Locate every Plasmodium falciparum-infected red blood cell.
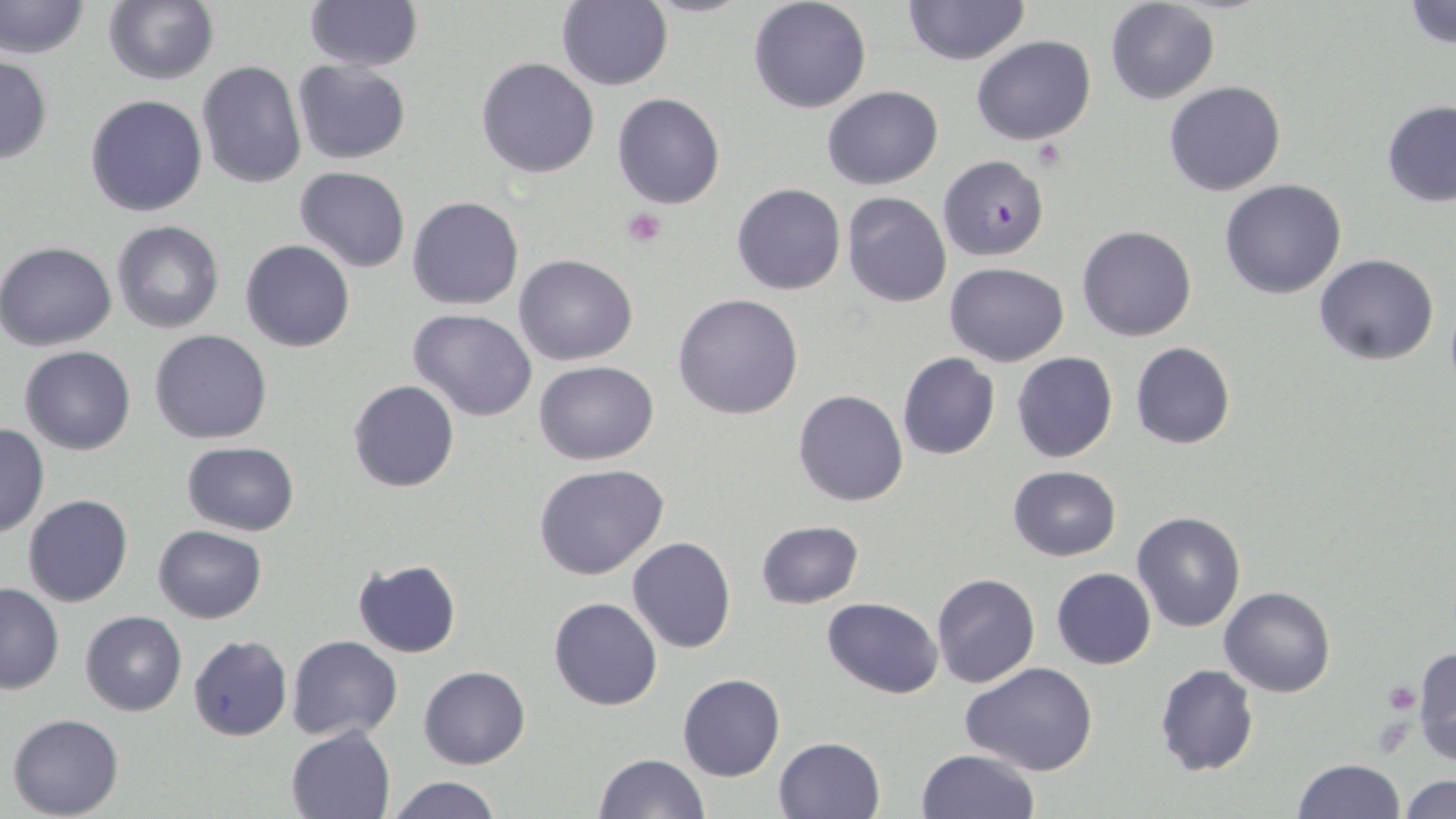

Approximate bounding boxes as (x1, y1, x2, y2) in pixels.
Plasmodium falciparum-infected red blood cells: (937, 155, 1049, 261).

slide-level diagnosis = Plasmodium falciparum
preparation = thin blood film
stain = May-Grünwald-Giemsa
image size = 1456×819 pixels
modality = optical microscopy
platelet locations = approximate bounding boxes as (x1, y1, x2, y2) in pixels: (622, 206, 666, 248), (1382, 680, 1421, 712)
uninfected red blood cell locations = approximate bounding boxes as (x1, y1, x2, y2) in pixels: (0, 0, 89, 60), (748, 0, 872, 113), (904, 0, 1029, 66), (303, 1, 422, 72), (556, 1, 672, 91), (1105, 1, 1219, 104), (1403, 1, 1456, 51), (102, 2, 218, 85), (971, 34, 1096, 144), (0, 53, 52, 163), (476, 57, 600, 178), (196, 59, 305, 188), (292, 61, 411, 164), (1164, 80, 1286, 196), (823, 86, 943, 189), (612, 93, 724, 208), (84, 94, 207, 216), (1381, 102, 1456, 206), (295, 165, 410, 273), (1218, 178, 1347, 299), (730, 182, 846, 295), (841, 192, 952, 308), (407, 195, 524, 310), (112, 221, 224, 334), (1077, 225, 1197, 342), (241, 240, 355, 352), (0, 241, 119, 351), (1314, 253, 1440, 366), (514, 254, 638, 366), (945, 262, 1069, 365), (673, 294, 804, 420), (408, 310, 538, 422), (150, 329, 274, 444), (1130, 342, 1236, 449), (19, 346, 136, 455), (896, 351, 1001, 460), (1011, 351, 1118, 463), (533, 360, 659, 464), (348, 380, 460, 493), (792, 389, 909, 508), (0, 420, 50, 539), (181, 442, 302, 536), (533, 463, 670, 580), (1008, 465, 1121, 560), (23, 494, 133, 608), (1132, 510, 1246, 631), (755, 519, 864, 608), (151, 524, 267, 624), (626, 536, 736, 655), (352, 559, 462, 658), (1051, 567, 1156, 668), (931, 572, 1040, 687), (0, 581, 64, 695), (1220, 586, 1335, 697), (548, 596, 663, 710), (823, 597, 943, 697), (80, 609, 187, 715), (188, 635, 292, 740), (286, 635, 402, 742), (1411, 647, 1456, 763), (960, 662, 1099, 777), (1154, 663, 1257, 776), (418, 665, 531, 769), (677, 674, 785, 781), (7, 713, 124, 819), (286, 725, 396, 818), (773, 736, 886, 819), (914, 749, 1040, 819), (593, 753, 708, 819), (1291, 758, 1405, 818), (1402, 774, 1456, 818), (385, 776, 506, 818)
magnification = 1000x
field of view = single